State the blood parasite species.
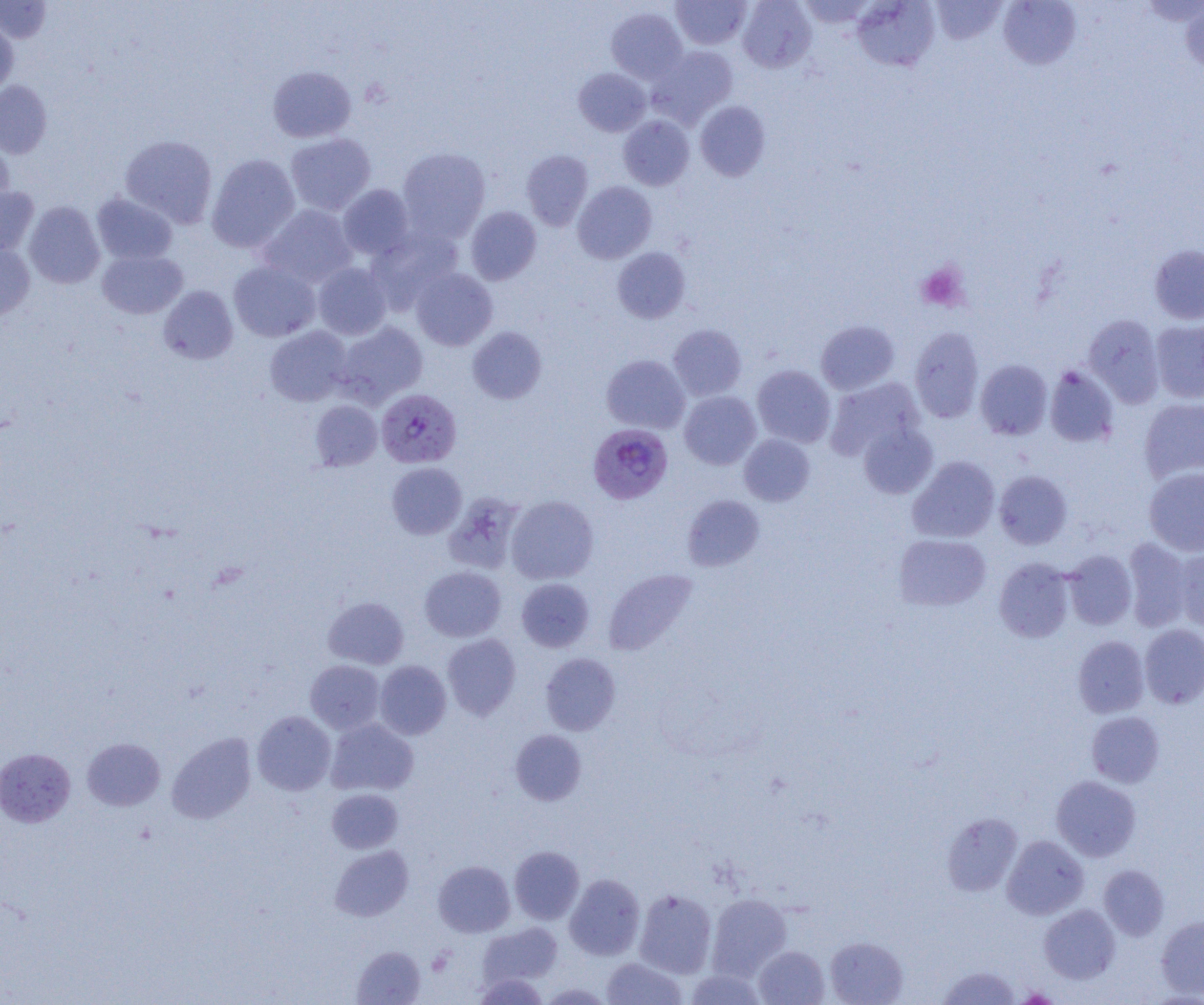

Plasmodium falciparum.

Summary:
  - Coordinate format: approximate bounding boxes as (x1,y1)-(x2,y2) corner pairs in pixels
  - Plasmodium falciparum-infected red blood cell locations: (376,388)-(461,468), (588,424)-(673,504)
  - Platelet locations: (915,261)-(969,312)
  - Uninfected red blood cell locations: (0,0)-(52,43), (671,0)-(751,49), (738,0)-(816,73), (797,0)-(877,29), (852,0)-(940,71), (930,0)-(1008,45), (998,0)-(1081,69), (1181,2)-(1204,75), (606,7)-(687,84), (0,20)-(18,96), (649,46)-(737,128), (268,65)-(356,142), (574,67)-(651,136), (0,81)-(52,158), (695,101)-(771,181), (618,115)-(694,190), (285,133)-(376,215), (120,135)-(217,228), (0,136)-(14,210), (398,148)-(490,241), (521,150)-(593,230), (206,154)-(300,253), (573,181)-(657,263), (338,184)-(415,260), (0,186)-(39,258), (92,192)-(178,265), (24,201)-(105,288), (259,204)-(357,288), (466,206)-(541,284), (366,226)-(463,311), (0,243)-(35,320), (1149,245)-(1204,324), (612,247)-(691,323), (97,250)-(187,318), (229,261)-(320,342), (313,262)-(391,339), (411,268)-(498,350), (158,286)-(238,364), (1083,314)-(1164,407), (816,320)-(900,395), (1151,320)-(1204,403), (335,321)-(428,407), (668,324)-(747,401), (265,326)-(352,406), (468,326)-(547,404), (909,327)-(984,423), (601,354)-(690,434), (975,359)-(1052,439), (752,365)-(835,447), (1044,365)-(1119,448), (825,377)-(925,462), (679,391)-(761,469), (1139,398)-(1204,484), (310,400)-(382,471), (858,422)-(938,499), (739,434)-(815,506), (907,456)-(1000,543), (386,462)-(466,539), (1144,467)-(1204,556), (994,470)-(1072,549), (444,492)-(524,574), (506,495)-(598,584), (682,495)-(765,571), (894,533)-(991,611), (1123,538)-(1193,632), (1174,547)-(1204,633), (1064,550)-(1137,630), (994,558)-(1074,643), (419,566)-(506,641), (603,568)-(698,656), (516,578)-(594,652), (323,596)-(408,669), (1139,624)-(1204,708), (442,634)-(521,720), (1073,635)-(1149,718), (540,653)-(620,735), (305,660)-(385,733), (375,660)-(451,739), (252,710)-(336,795), (1086,711)-(1165,787), (326,719)-(418,796), (510,729)-(587,805), (167,732)-(256,823), (82,738)-(165,810), (0,748)-(76,827), (1051,775)-(1141,862), (327,788)-(403,854), (941,813)-(1022,896), (1002,835)-(1089,919), (330,845)-(413,921), (509,846)-(584,924), (433,861)-(515,937), (1099,865)-(1169,940), (565,874)-(645,960), (634,889)-(717,978), (706,893)-(792,980), (1039,905)-(1120,983), (1156,914)-(1204,998), (478,922)-(562,988), (825,936)-(908,1005), (352,945)-(426,1004), (754,945)-(829,1005), (601,957)-(687,1004), (938,965)-(1021,1005), (685,970)-(767,1005), (472,973)-(549,1004), (538,982)-(614,1004)
  - Preparation: thin blood film
  - Image size: 1204×1005 pixels
  - Modality: optical microscopy
  - Field of view: single
  - Magnification: 1000x